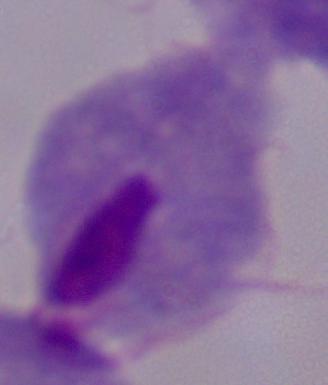
Summary:
  - Identification: trichomonad
  - Magnification: 1000x
  - Modality: micrograph